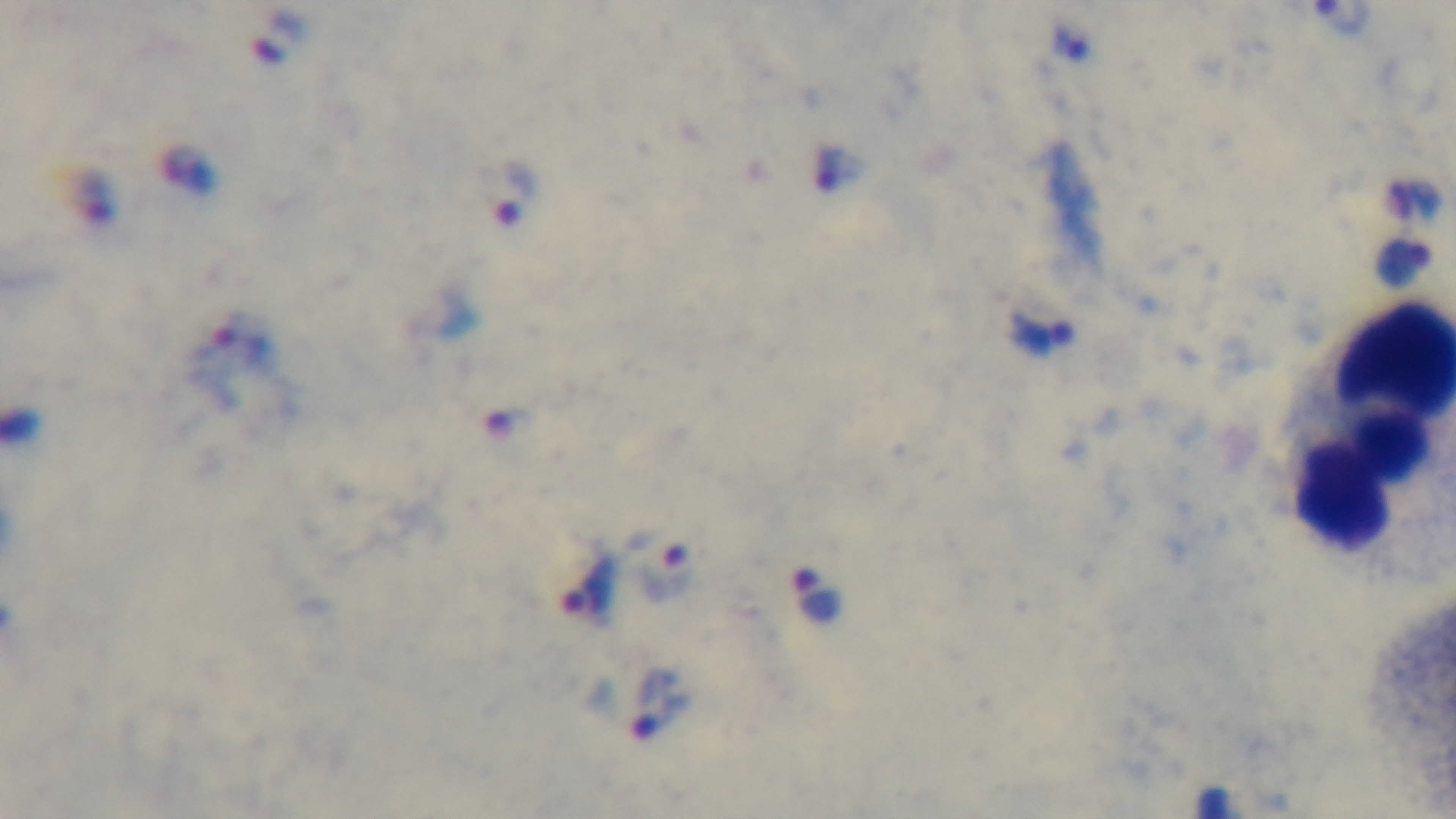

{
  "malaria_status": "infected",
  "objective": "100x oil immersion",
  "capture": "mounted 4K digital camera",
  "preparation": "thick",
  "field_of_view": "single",
  "stain": "Giemsa",
  "modality": "light microscopy"
}